State which cell type is depicted.
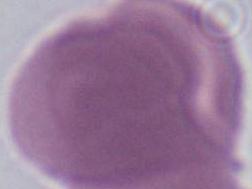

This is an erythrocyte.

Summary:
  - Magnification: 1000x
  - Modality: photomicrograph